Report the malaria status of this cell.
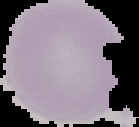
It is uninfected.

Summary:
  - Image size: 139×127 pixels
  - Image type: cell region segmented out of the field of view; surrounding area masked to black
  - Preparation: thin blood smear